Report the malaria status of this cell.
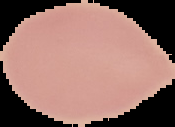

Uninfected.

preparation = thin blood smear
image type = segmented cell region with the area outside set to black
image size = 175×127 pixels